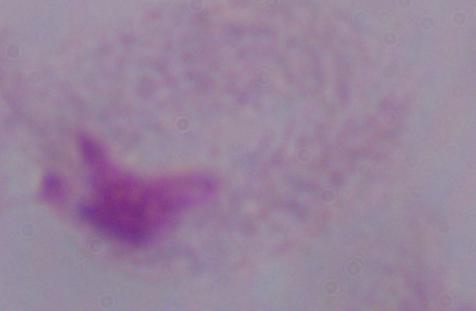
identification = trichomonad
magnification = 1000x
modality = micrograph